Report the malaria status of this cell.
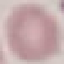

Uninfected.

Thin blood film. Automatically extracted cell patch, resized to 64 × 64 pixels. Giemsa-stained preparation. Photographed with a smartphone camera at the microscope eyepiece.